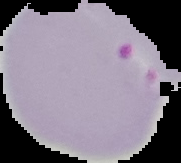

Malaria status: parasitized. From a thin blood smear. Image is 181×163 pixels. Segmented cell region on a black background.